Report the malaria status of this cell.
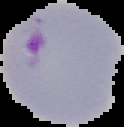
Parasitized.

Summary:
  - Preparation: thin blood film
  - Image type: cell region segmented out of the field of view; surrounding area masked to black
  - Image size: 124×127 pixels